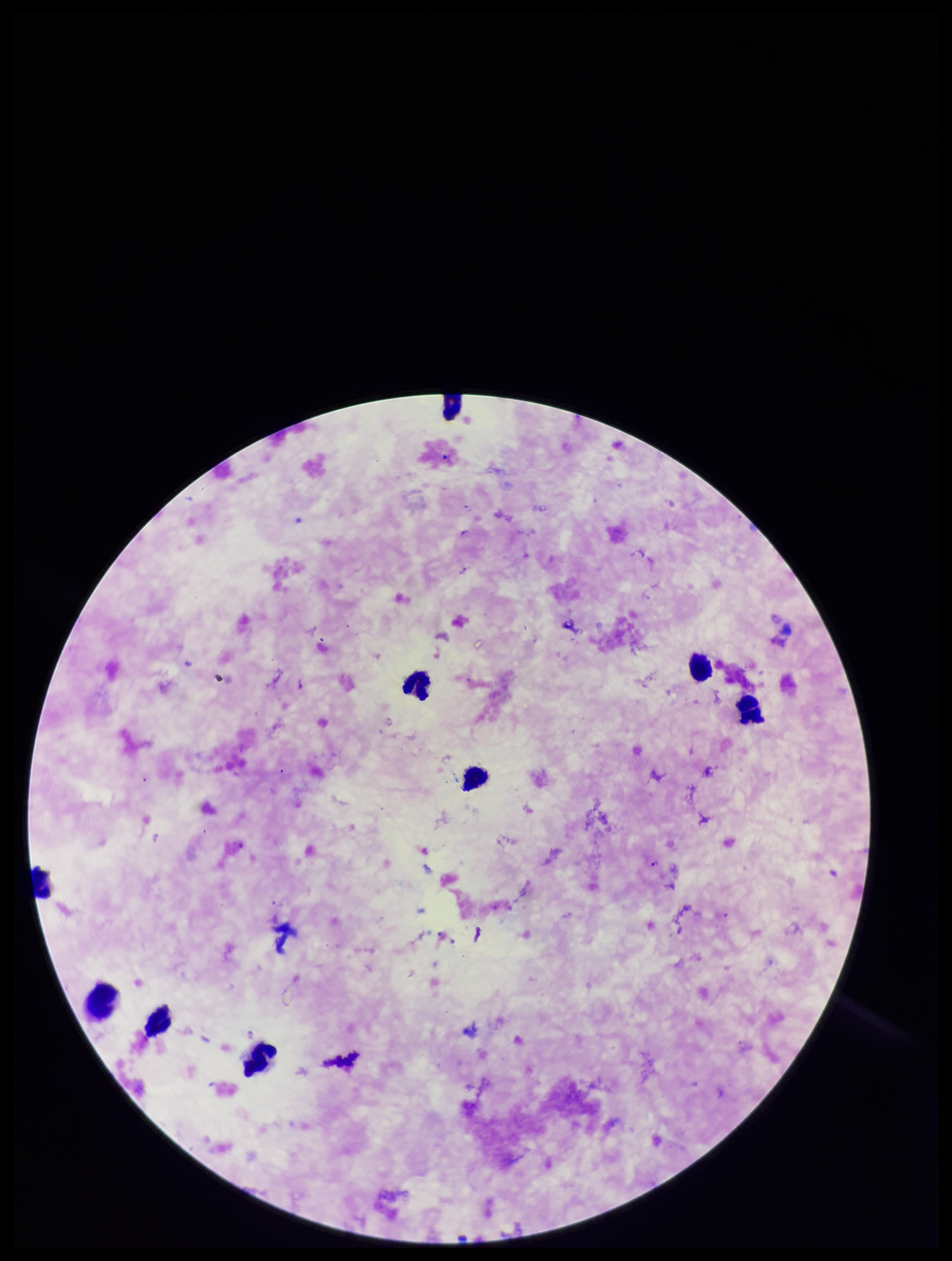 Parasite count: 1. Image is 952×1261 pixels. Single field of view. Species reported for this patient: Plasmodium falciparum. Leukocyte count: 9. Patient malaria status: positive. Photographed through the microscope eyepiece with a smartphone camera. Plasmodium parasites: identified. Preparation: thick. Stained with Giemsa.